Assess this cell for malaria.
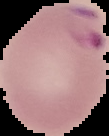

Parasitized.

Summary:
  - Image type: cell region segmented out of the field of view; surrounding area masked to black
  - Preparation: thin blood film
  - Image size: 109×136 pixels